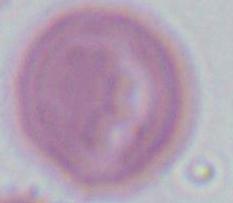

identification = red blood cell
modality = micrograph
magnification = 1000x